Classify this cell by malaria status.
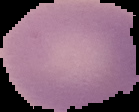

It is uninfected.

Image is 139×112 pixels. From a thin blood film. Segmented cell region on a black background.